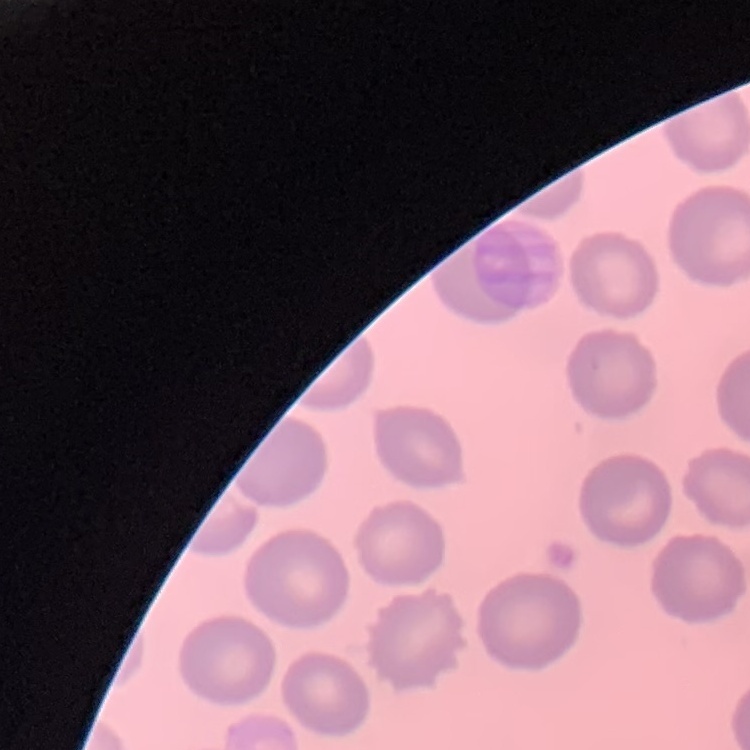 The red blood cells show no rouleaux formation. Thin peripheral smear. Field's or Giemsa stain. One tile cut from a larger photomicrograph.